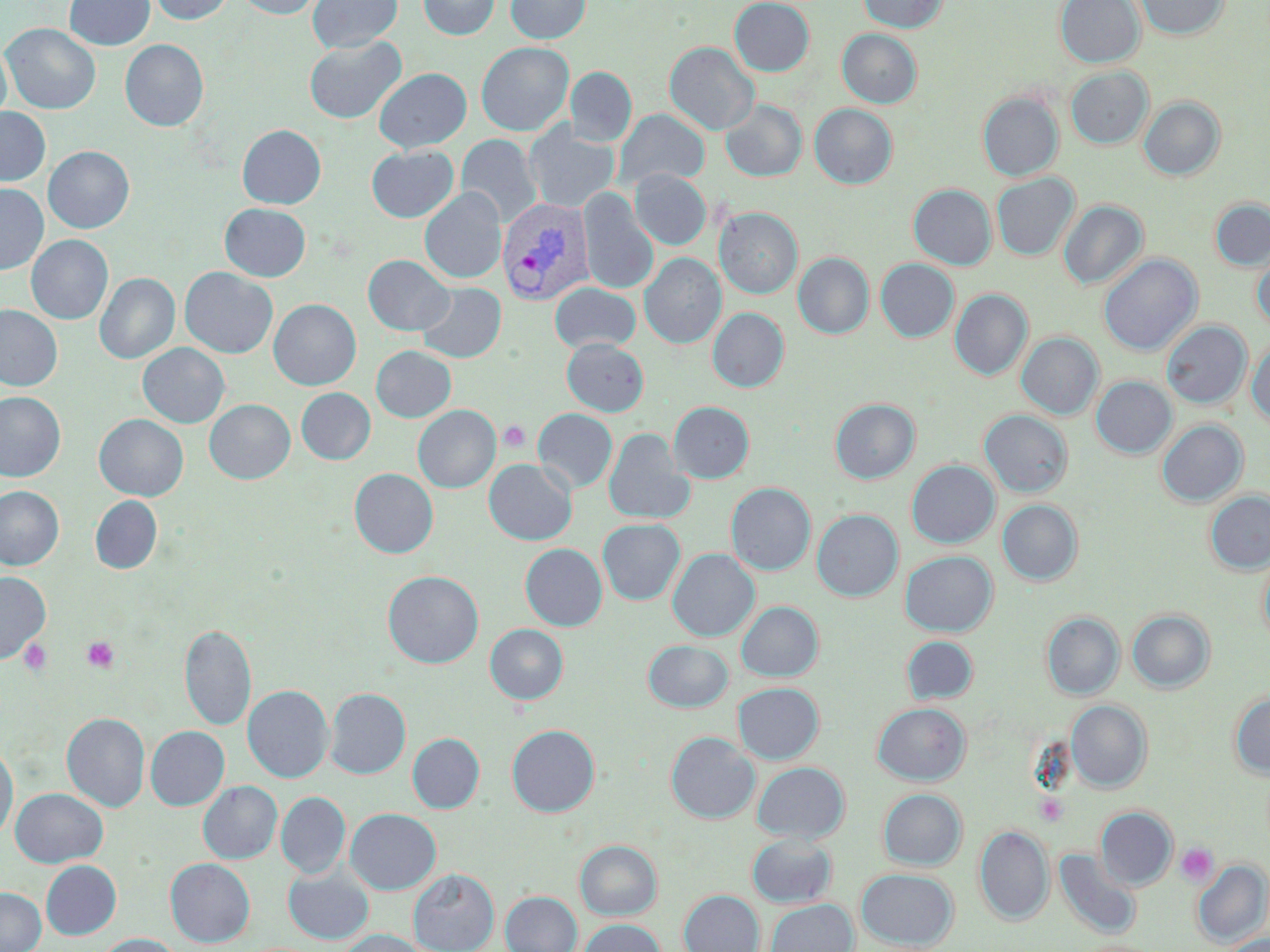 Approximate bounding boxes as [x1, y1, x2, y2] in pixels. Platelet locations: [498, 421, 530, 453], [81, 636, 121, 674], [19, 638, 53, 676], [1176, 842, 1219, 887]. Plasmodium vivax-infected red blood cell locations: [497, 197, 593, 305]. Uninfected red blood cell locations: [64, 0, 154, 51], [147, 0, 235, 25], [235, 0, 323, 19], [307, 0, 402, 53], [418, 0, 499, 40], [505, 0, 591, 43], [729, 0, 814, 76], [858, 0, 948, 33], [1055, 0, 1144, 68], [1135, 0, 1230, 40], [2, 22, 101, 114], [837, 29, 922, 108], [303, 36, 406, 124], [120, 39, 208, 131], [0, 41, 12, 126], [476, 42, 574, 135], [664, 42, 760, 135], [565, 66, 636, 146], [1065, 67, 1153, 150], [374, 68, 471, 152], [978, 91, 1064, 181], [1139, 96, 1225, 180], [720, 99, 807, 182], [809, 104, 897, 189], [0, 107, 51, 186], [614, 109, 709, 189], [524, 123, 619, 212], [237, 124, 326, 208], [456, 134, 542, 227], [366, 145, 459, 222], [43, 146, 134, 233], [630, 169, 711, 250], [991, 173, 1079, 260], [0, 183, 49, 275], [908, 184, 996, 270], [420, 188, 506, 283], [578, 190, 659, 294], [1210, 198, 1270, 271], [1059, 200, 1147, 290], [220, 203, 311, 281], [714, 207, 803, 299], [26, 235, 113, 324], [1252, 250, 1270, 331], [793, 252, 874, 339], [640, 253, 726, 349], [1099, 254, 1202, 355], [363, 255, 454, 336], [876, 258, 959, 342], [180, 267, 278, 358], [95, 273, 180, 364], [550, 282, 640, 354], [417, 283, 506, 363], [950, 289, 1033, 380], [269, 299, 361, 390], [0, 304, 62, 391], [708, 307, 789, 392], [1161, 321, 1251, 408], [1016, 332, 1103, 419], [1247, 338, 1270, 427], [562, 339, 649, 416], [138, 343, 230, 428], [371, 346, 456, 422], [1091, 376, 1177, 458], [296, 388, 376, 464], [0, 391, 65, 481], [830, 398, 920, 483], [204, 399, 295, 484], [668, 401, 754, 483], [413, 405, 500, 492], [533, 408, 618, 493], [979, 409, 1073, 497], [94, 413, 188, 501], [1156, 420, 1247, 507], [603, 428, 693, 524], [484, 459, 576, 545], [907, 460, 999, 548], [349, 468, 438, 558], [726, 482, 815, 574], [0, 486, 64, 570], [1205, 490, 1270, 574], [90, 495, 162, 574], [997, 499, 1082, 585], [811, 509, 903, 601], [598, 518, 685, 605], [520, 543, 607, 630], [668, 548, 759, 641], [1258, 549, 1270, 651], [900, 550, 997, 636], [383, 570, 483, 668], [0, 571, 51, 663], [737, 601, 823, 681], [1126, 609, 1215, 693], [1042, 612, 1124, 699], [179, 624, 256, 732], [485, 624, 568, 704], [901, 636, 978, 704], [643, 640, 733, 712], [733, 682, 823, 764], [244, 685, 333, 782], [325, 687, 410, 779], [1229, 689, 1270, 779], [1066, 699, 1152, 792], [872, 702, 970, 784], [61, 712, 149, 813], [507, 725, 600, 816], [146, 727, 229, 810], [666, 731, 759, 823], [407, 733, 484, 813], [0, 741, 18, 844], [752, 761, 850, 842], [199, 781, 282, 863], [10, 788, 108, 867], [878, 789, 966, 870], [276, 791, 350, 878], [1096, 807, 1177, 890], [346, 808, 440, 894], [974, 825, 1053, 925], [746, 835, 838, 908], [575, 840, 662, 919], [1053, 847, 1142, 940], [165, 858, 254, 947], [41, 860, 121, 940], [1192, 860, 1269, 946], [283, 867, 373, 943], [409, 868, 499, 952], [856, 868, 958, 949], [0, 888, 46, 951], [679, 889, 764, 952], [500, 891, 582, 952], [765, 899, 858, 952], [578, 918, 665, 952], [337, 929, 428, 952], [1220, 933, 1270, 952], [96, 934, 184, 952]. Slide-level diagnosis: Plasmodium vivax. Image is 1270×952 pixels. One field of a larger specimen. Thin blood film. Light microscopy. 1000x magnification. May-Grünwald-Giemsa stain.